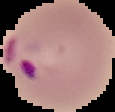

result = malaria parasites detected
preparation = thin blood smear
image type = segmented cell region on a black background
image size = 115×112 pixels